Point out each Plasmodium parasite and each leukocyte.
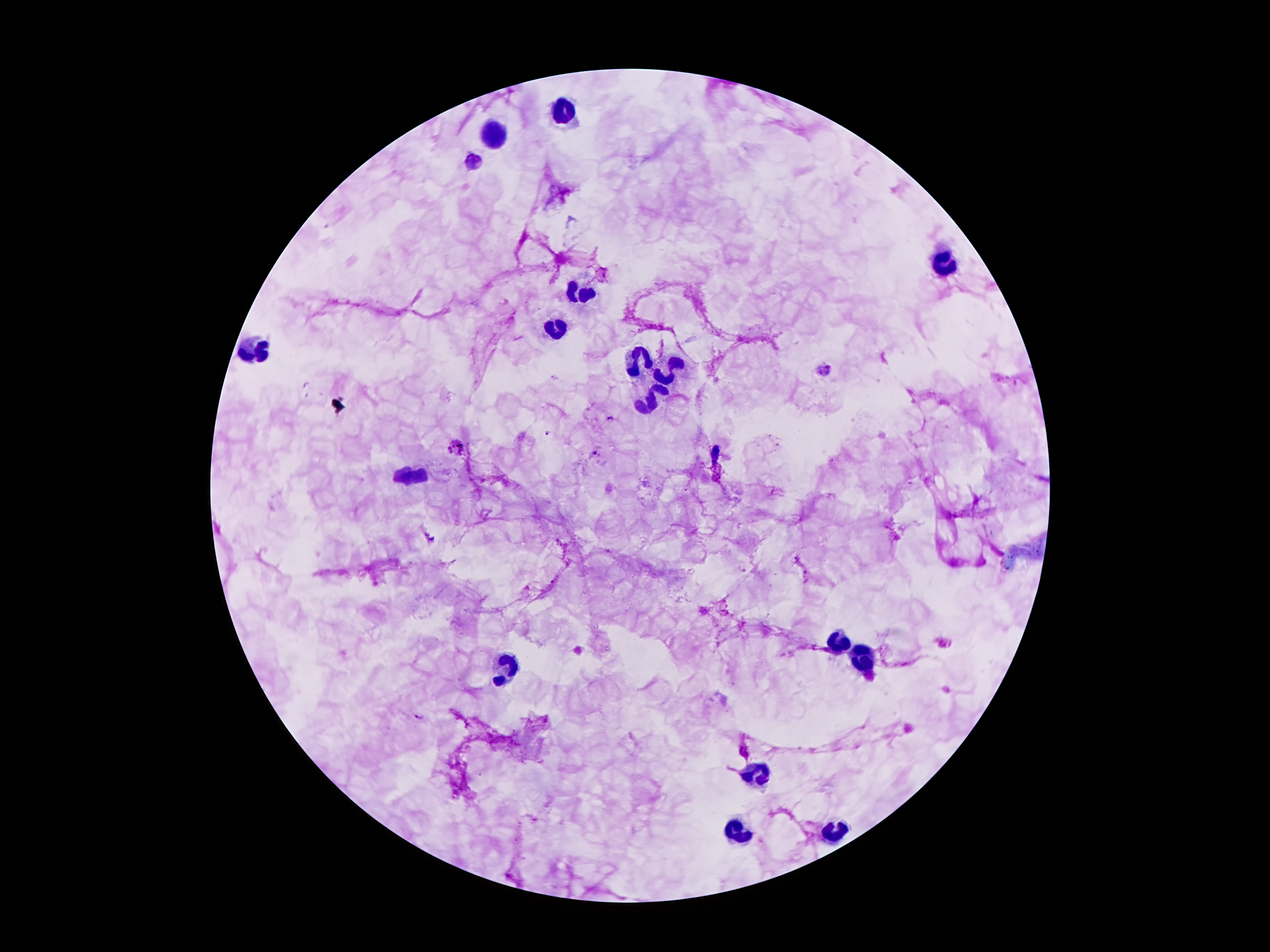

Approximate centers as {x, y} in pixels.
Plasmodium parasites: {474, 161}, {823, 370}, {610, 418}, {550, 434}, {455, 447}, {596, 454}, {418, 717}.
Leukocytes: {563, 112}, {497, 134}, {943, 263}, {578, 294}, {559, 330}, {258, 349}, {639, 358}, {669, 370}, {652, 399}, {416, 475}, {839, 641}, {860, 662}, {507, 667}, {762, 771}, {739, 830}, {834, 833}.

image_size: 1270×952 pixels
stain: Giemsa
preparation: thick blood film
field_of_view: single
magnification: 100x
capture: smartphone camera through the microscope eyepiece
patient_malaria_status: infected with Plasmodium falciparum